Classify this cell by malaria status.
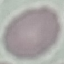
It is uninfected.

capture = smartphone through the microscope eyepiece
preparation = thin blood smear
image type = automatically extracted cell patch, resized to 64 × 64 pixels
stain = Giemsa